Report the malaria status of this cell.
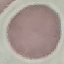
It is uninfected.

Summary:
  - Image type: cell patch, automatically extracted from a larger field of view and resized to 64 × 64 pixels
  - Capture: smartphone camera at the microscope eyepiece
  - Stain: Giemsa
  - Preparation: thin blood smear